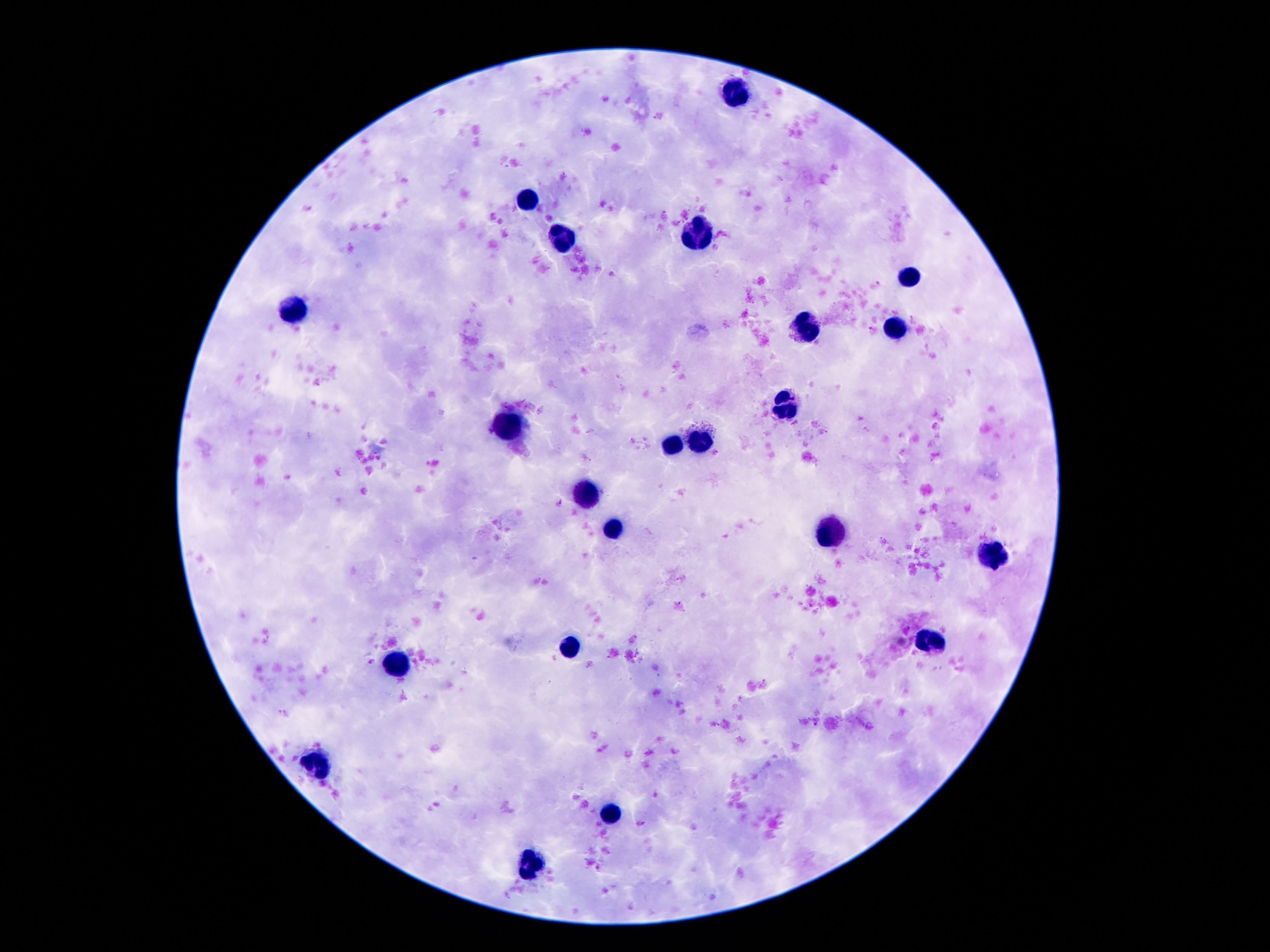

capture = smartphone camera through the microscope eyepiece
image size = 1270×952 pixels
field of view = one from this slide
patient malaria status = uninfected
preparation = thick blood smear
stain = Giemsa
leukocyte locations = approximate object centers, in pixels from the top-left corner: (x=734, y=89), (x=529, y=200), (x=699, y=235), (x=558, y=237), (x=907, y=277), (x=294, y=306), (x=806, y=328), (x=894, y=331), (x=783, y=407), (x=511, y=422), (x=702, y=445), (x=675, y=447), (x=586, y=489), (x=613, y=531), (x=828, y=533), (x=991, y=556), (x=932, y=640), (x=568, y=647), (x=395, y=662), (x=314, y=763), (x=613, y=813), (x=536, y=868)
magnification = 100x